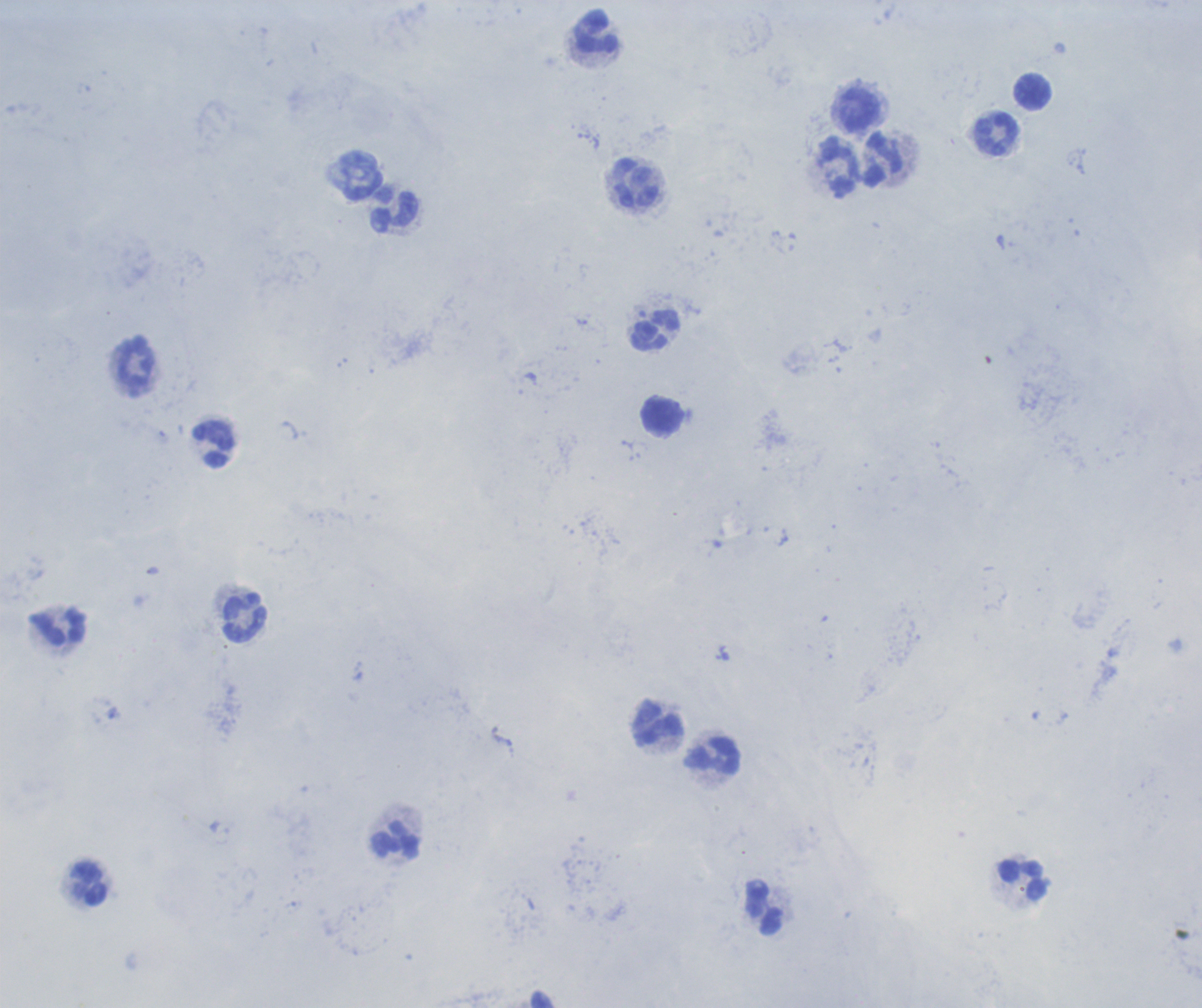

Approximate centers as {x, y} in pixels. Leukocyte locations: {594, 32}, {1033, 93}, {860, 110}, {996, 136}, {883, 161}, {839, 168}, {636, 184}, {394, 210}, {655, 330}, {663, 417}, {215, 444}, {244, 618}, {57, 626}, {658, 723}, {714, 756}, {396, 842}, {1023, 880}, {89, 884}, {764, 909}. One field from this slide. Captured at 100x magnification. Previously used in an actual diagnosis. Thick smear of blood. Image is 1202×1008 pixels. Result: negative for malaria parasites. Background quality: unsatisfactory. Romanowsky-stained preparation.